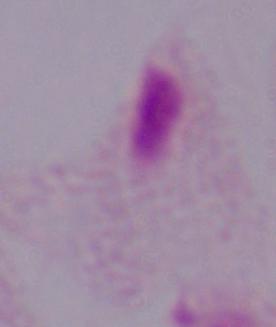

magnification = 1000x
modality = micrograph
identification = trichomonad